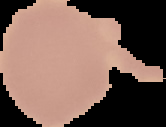
From a thin blood smear. The area outside the segmented cell region is set to black. Image is 166×127 pixels. Malaria status: uninfected.